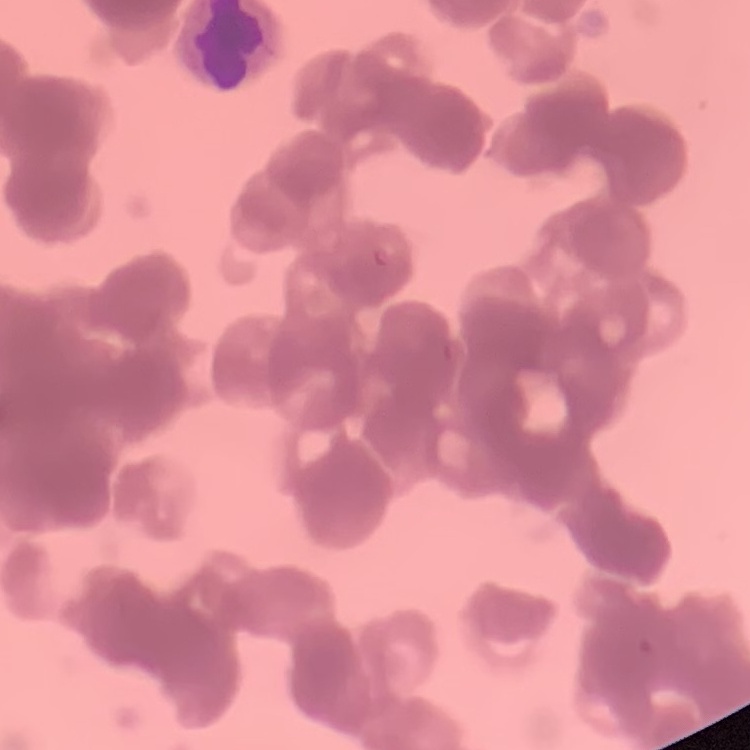
Summary:
  - Red blood cell morphology: rouleaux formation
  - Preparation: thin blood film
  - Stain: Field's or Giemsa
  - Image type: square crop of a larger photomicrograph